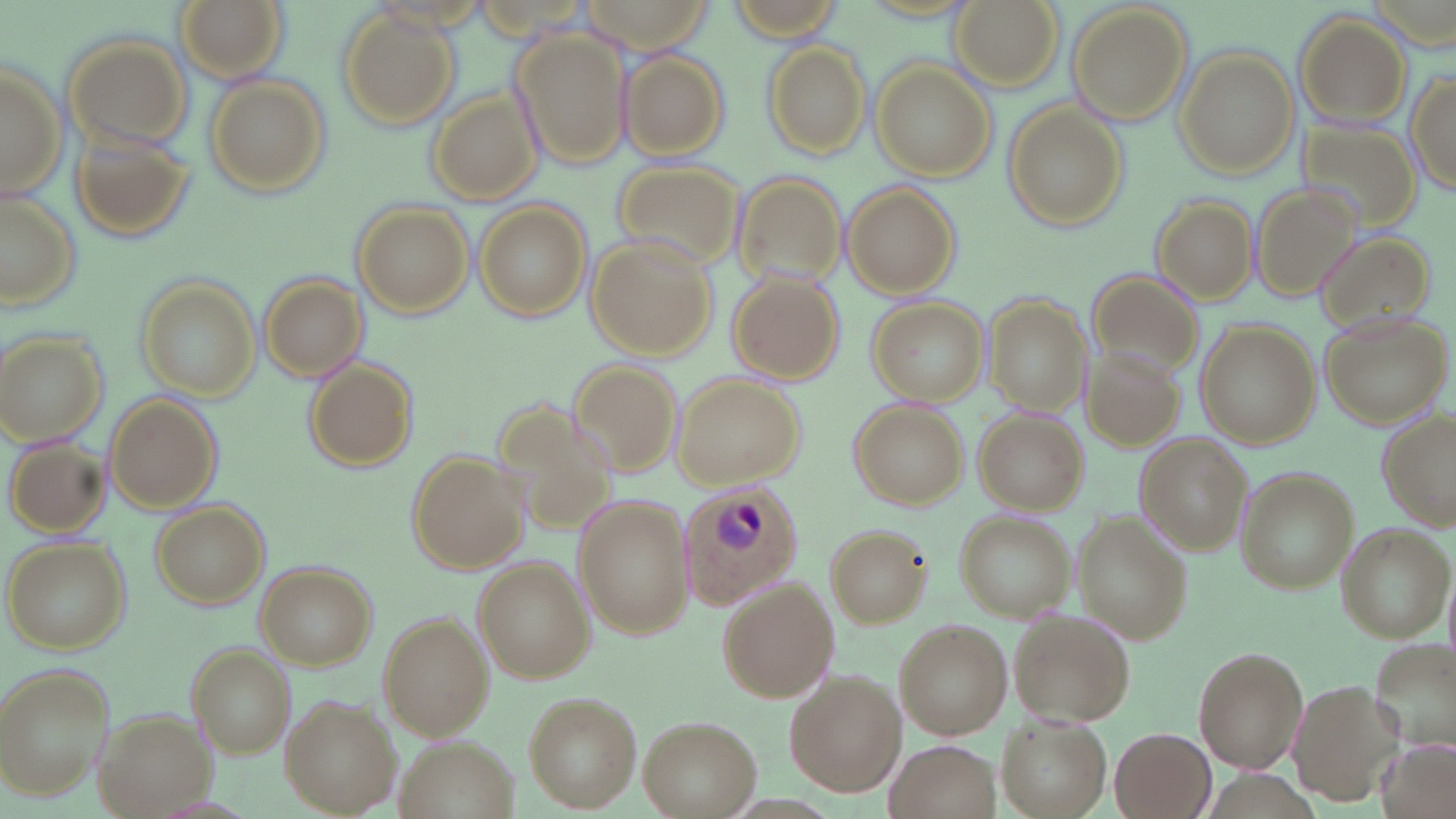
slide_level_diagnosis: Plasmodium ovale
preparation: thin blood film
stain: May-Grünwald-Giemsa
modality: optical microscopy
plasmodium_ovale_infected_red_blood_cell_locations: 'approximate bounding boxes as (x1,y1)-(x2,y2) corner pairs in pixels: (677,482)-(805,607)'
magnification: 1000x
uninfected_red_blood_cell_locations: 'approximate bounding boxes as (x1,y1)-(x2,y2) corner pairs in pixels: (176,0)-(287,81), (581,0)-(716,63), (949,0)-(1062,92), (1068,4)-(1192,124), (336,6)-(461,130), (1295,12)-(1410,127), (512,29)-(629,168), (64,33)-(191,147), (764,41)-(872,159), (1173,47)-(1298,179), (619,49)-(731,160), (0,59)-(67,200), (872,60)-(996,181), (1407,67)-(1455,198), (203,73)-(330,199), (427,93)-(540,204), (1004,102)-(1125,231), (1292,114)-(1427,241), (73,126)-(200,240), (610,160)-(745,269), (732,168)-(850,286), (841,182)-(959,298), (1248,183)-(1359,304), (0,190)-(81,310), (1151,194)-(1259,306), (475,201)-(591,321), (351,202)-(473,318), (1313,230)-(1436,337), (584,237)-(715,359), (1080,266)-(1210,383), (729,270)-(843,383), (136,274)-(261,406), (261,274)-(368,381), (867,297)-(987,404), (986,297)-(1091,416), (1324,315)-(1451,426), (1198,319)-(1318,447), (0,330)-(107,444), (1078,344)-(1188,456), (572,358)-(684,473), (306,359)-(419,470), (676,373)-(805,488), (106,394)-(223,512), (489,395)-(621,540), (849,401)-(970,510), (976,409)-(1088,514), (1378,412)-(1456,530), (1137,437)-(1249,553), (5,438)-(110,537), (405,451)-(527,574), (1232,464)-(1355,594), (574,496)-(694,640), (150,498)-(271,608), (955,511)-(1076,621), (1075,516)-(1190,643), (824,523)-(931,629), (1337,525)-(1451,641), (4,536)-(131,654), (475,558)-(594,682), (255,562)-(376,670), (718,578)-(838,704), (1006,608)-(1134,727), (380,612)-(496,738), (895,619)-(1012,737), (1370,637)-(1456,751), (189,644)-(296,758), (1193,648)-(1307,773), (2,663)-(116,801), (784,670)-(906,796), (1287,679)-(1401,808), (523,692)-(642,811), (281,696)-(400,816), (98,709)-(213,817), (639,715)-(760,817), (996,715)-(1111,818), (1111,728)-(1215,819), (394,735)-(517,819), (883,738)-(1003,819), (1380,739)-(1456,819)'
field_of_view: single
image_size: 1456×819 pixels